Outline each uninfected red blood cell.
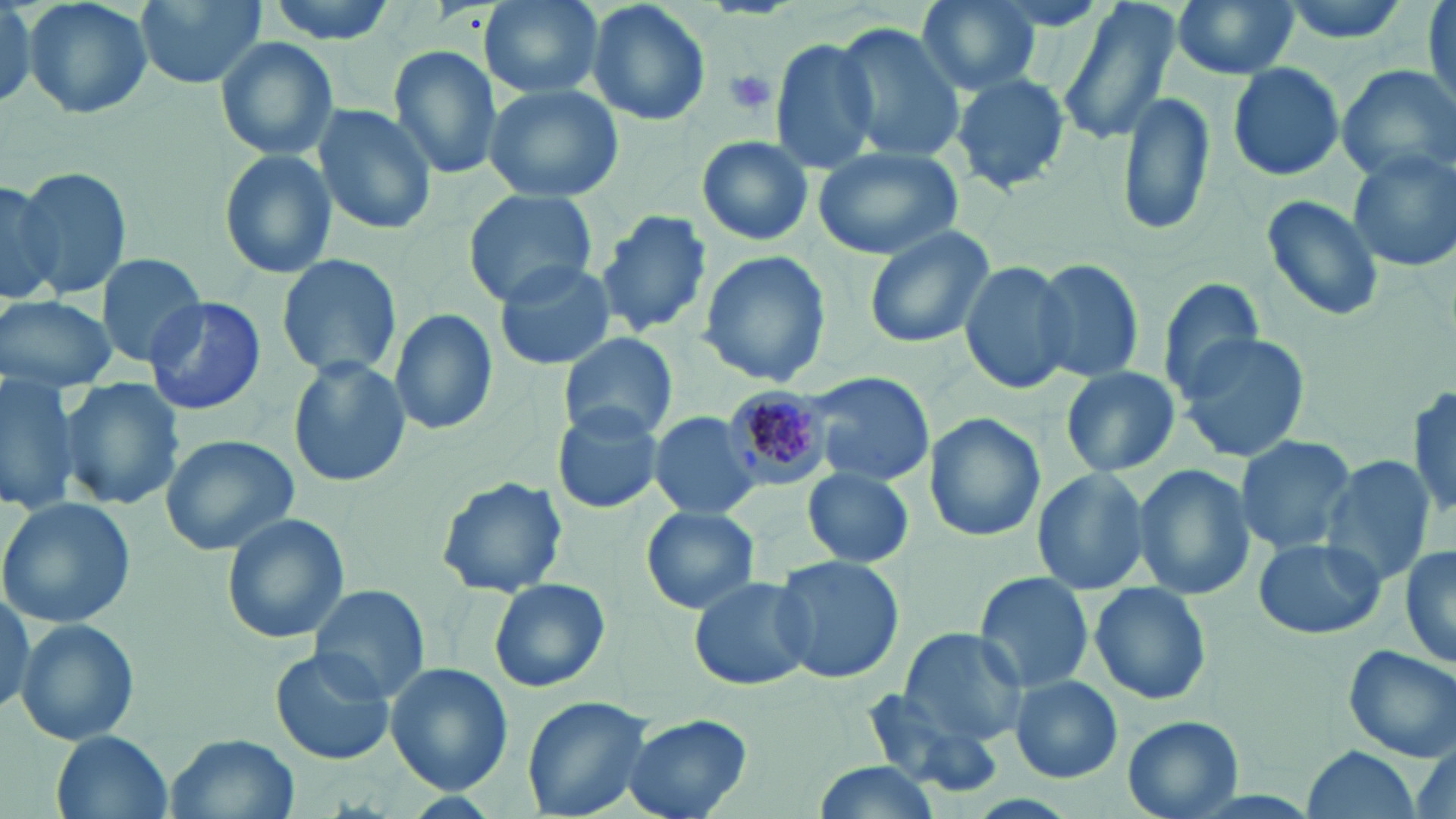

Approximate bounding boxes as [x1, y1, x2, y2] in pixels.
Uninfected red blood cells: [22, 0, 153, 121], [132, 0, 268, 90], [258, 0, 404, 43], [480, 0, 605, 101], [586, 0, 710, 127], [914, 0, 1041, 95], [1055, 0, 1179, 148], [1171, 0, 1298, 79], [1271, 0, 1418, 46], [1422, 1, 1456, 108], [0, 2, 36, 105], [832, 23, 966, 165], [214, 35, 339, 162], [769, 38, 882, 174], [387, 45, 501, 182], [1226, 61, 1345, 181], [1336, 64, 1455, 181], [947, 70, 1071, 195], [483, 81, 626, 204], [1116, 89, 1214, 238], [310, 102, 439, 234], [697, 135, 813, 246], [811, 143, 963, 259], [217, 147, 335, 280], [1347, 150, 1456, 272], [12, 165, 130, 302], [0, 178, 62, 305], [463, 190, 598, 306], [1260, 193, 1386, 322], [596, 208, 713, 339], [862, 226, 995, 349], [697, 249, 833, 387], [95, 251, 210, 366], [274, 253, 402, 381], [1027, 256, 1146, 385], [493, 258, 617, 371], [959, 258, 1078, 396], [1152, 278, 1265, 401], [0, 295, 118, 390], [142, 296, 265, 414], [388, 308, 499, 435], [1173, 331, 1312, 464], [558, 332, 679, 441], [287, 355, 411, 489], [1060, 366, 1181, 477], [804, 371, 937, 487], [0, 376, 84, 513], [59, 378, 186, 510], [1410, 385, 1456, 522], [549, 401, 668, 516], [647, 411, 764, 521], [922, 413, 1046, 543], [159, 434, 299, 555], [1234, 434, 1357, 554], [1318, 455, 1434, 584], [1132, 462, 1254, 601], [1029, 466, 1151, 595], [803, 470, 915, 567], [435, 475, 569, 597], [0, 497, 137, 629], [640, 507, 761, 615], [220, 512, 349, 644], [1251, 537, 1386, 641], [1400, 539, 1456, 675], [769, 555, 906, 685], [974, 573, 1095, 692], [687, 574, 814, 692], [486, 577, 611, 694], [1090, 581, 1212, 706], [309, 584, 430, 705], [16, 617, 140, 746], [899, 628, 1028, 745], [1343, 644, 1456, 761], [268, 647, 397, 765], [385, 662, 513, 794], [1010, 675, 1122, 783], [859, 690, 1005, 798], [520, 694, 656, 819], [621, 712, 753, 819], [1122, 717, 1244, 818], [50, 731, 172, 819], [166, 732, 296, 818], [1304, 745, 1420, 819], [808, 761, 947, 819].

slide-level diagnosis = Plasmodium malariae
image size = 1456×819 pixels
field of view = one of a larger specimen
preparation = thin blood smear
stain = May-Grünwald-Giemsa
magnification = 1000x
Plasmodium malariae-infected red blood cell locations = approximate bounding boxes as [x1, y1, x2, y2] in pixels: [721, 386, 832, 492]
platelet locations = approximate bounding boxes as [x1, y1, x2, y2] in pixels: [723, 69, 776, 115]
modality = optical microscopy